Outline every Plasmodium parasite, every leukocyte, and every artifact (stain precipitate or debris).
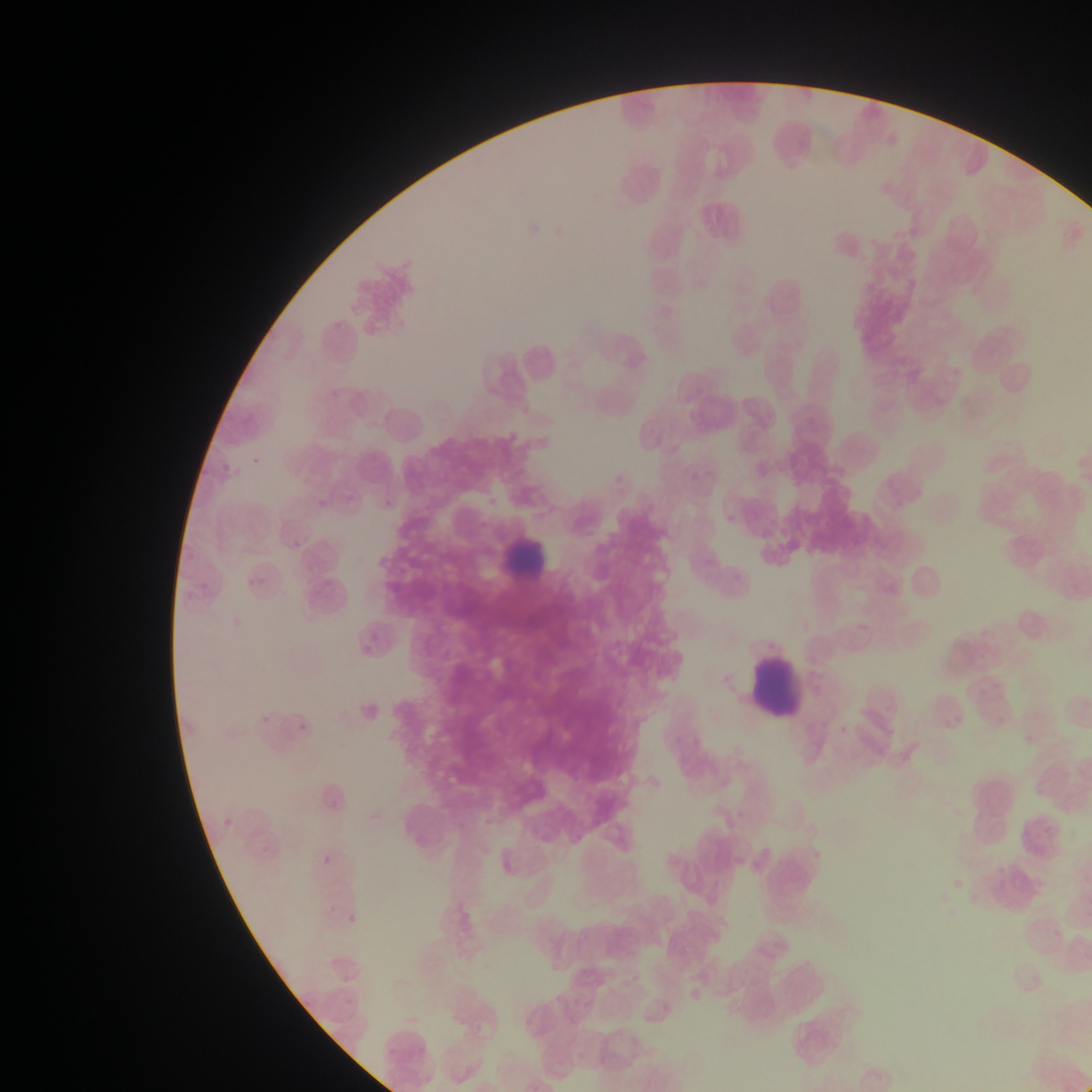

Approximate bounding boxes as (left, top, right, bottom) in pixels.
No Plasmodium parasites observed.
Leukocytes: (498, 517, 556, 579), (742, 662, 813, 714).

Photographed through a microscope with a mobile-phone camera. One field of view. Collected in Ghana. Thin blood smear. Image is 1092×1092 pixels.